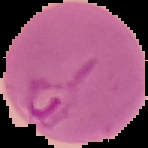 Malaria status: parasitized. From a thin blood film. Segmented cell region on a black background. Image is 148×148 pixels.